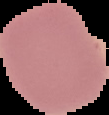

Summary:
  - Image size: 109×115 pixels
  - Image type: segmented cell region on a black background
  - Preparation: thin blood film
  - Malaria status: uninfected